State the blood parasite species.
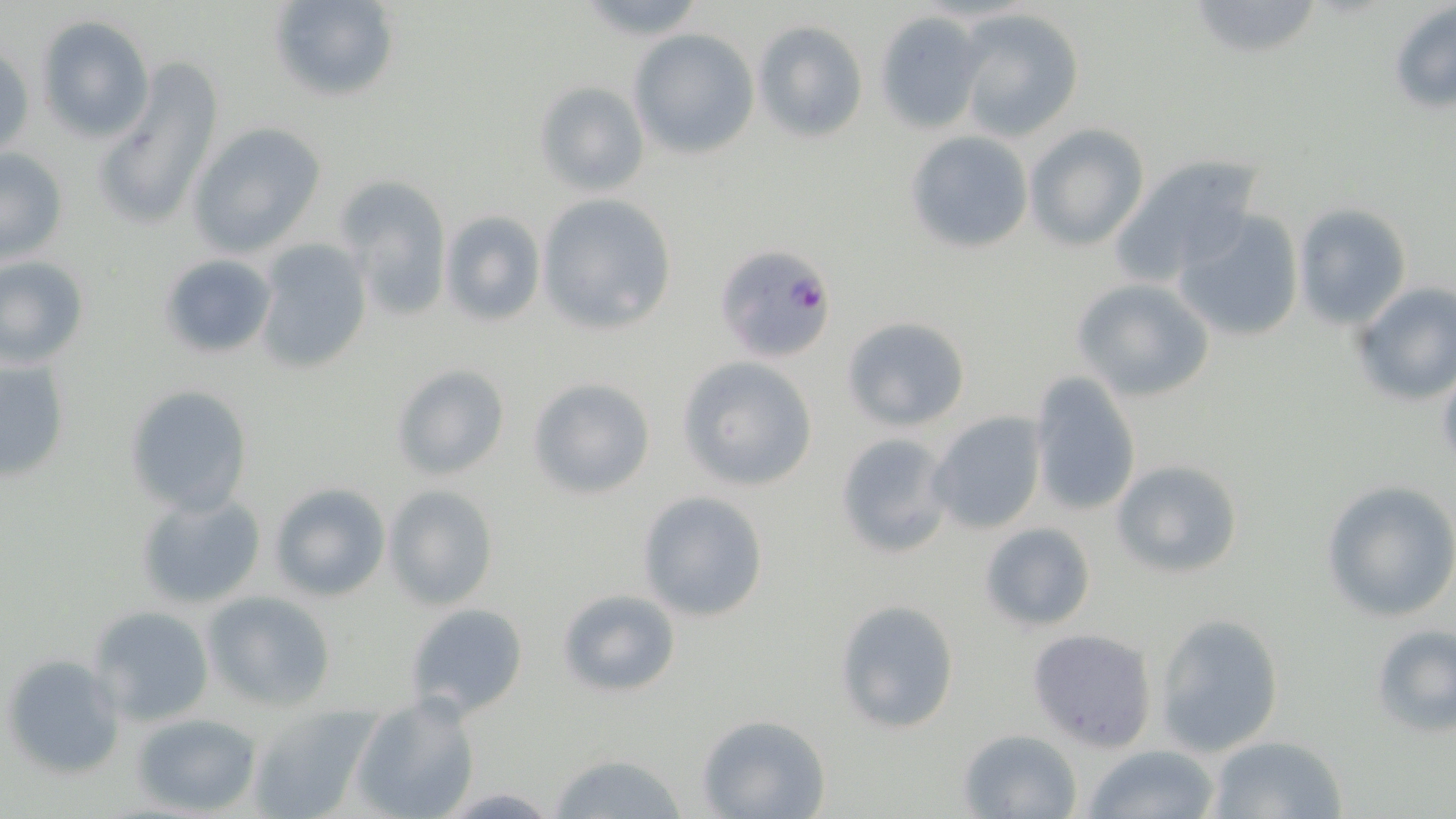

Plasmodium falciparum.

Approximate bounding boxes as [x1, y1, x2, y2] in pixels. Plasmodium falciparum-infected red blood cell locations: [715, 243, 837, 362]. Uninfected red blood cell locations: [263, 0, 401, 105], [1187, 0, 1322, 61], [1388, 2, 1456, 115], [951, 8, 1086, 142], [874, 12, 984, 133], [35, 15, 155, 143], [753, 19, 867, 141], [629, 28, 759, 158], [1, 43, 32, 159], [93, 59, 224, 232], [535, 81, 648, 196], [187, 121, 326, 257], [1023, 123, 1150, 252], [905, 129, 1034, 254], [0, 147, 69, 266], [1112, 153, 1266, 283], [340, 180, 450, 321], [537, 193, 678, 336], [1293, 203, 1411, 329], [439, 209, 545, 325], [1172, 210, 1305, 343], [253, 239, 372, 377], [156, 252, 278, 360], [1, 255, 90, 368], [1071, 277, 1215, 402], [1351, 281, 1456, 406], [841, 316, 971, 432], [0, 353, 72, 483], [678, 357, 817, 490], [391, 362, 511, 482], [1026, 373, 1141, 518], [528, 378, 656, 500], [123, 383, 254, 516], [928, 410, 1048, 535], [834, 432, 954, 559], [1110, 458, 1243, 579], [1320, 481, 1456, 623], [268, 483, 391, 602], [383, 484, 499, 611], [637, 490, 769, 622], [135, 492, 267, 610], [979, 522, 1096, 633], [555, 586, 681, 699], [203, 591, 335, 711], [834, 599, 962, 736], [403, 603, 529, 721], [91, 606, 214, 726], [1154, 612, 1284, 758], [1370, 623, 1456, 738], [1027, 628, 1158, 753], [2, 653, 125, 780], [352, 696, 480, 819], [247, 703, 379, 819], [133, 712, 262, 816], [695, 714, 832, 819], [958, 728, 1084, 819], [1206, 733, 1349, 819], [1082, 745, 1222, 819], [549, 752, 690, 819]. Optical microscopy. Single field of view. Image is 1456×819 pixels. Captured at 1000x magnification. May-Grünwald-Giemsa stain. Thin blood smear.